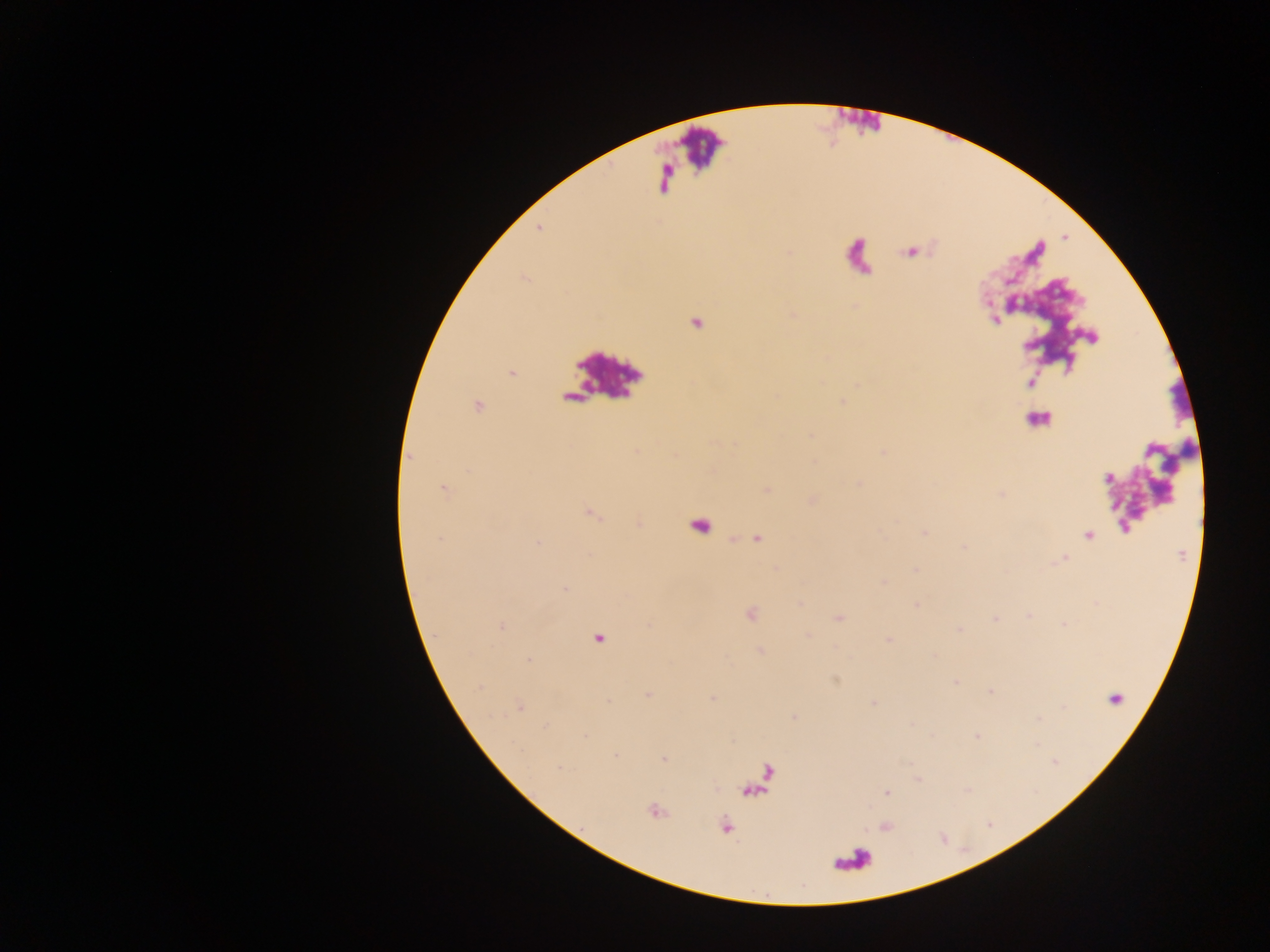
preparation = thick blood smear
Plasmodium parasite locations = approximate centers as (x, y) in pixels: (538, 227), (511, 373), (477, 406), (442, 488), (766, 490), (590, 512), (924, 533), (1088, 535), (757, 537), (1064, 559), (915, 568), (566, 589), (916, 604), (750, 613), (838, 616), (501, 626), (599, 638), (888, 640), (956, 681), (989, 691), (647, 694), (712, 697), (1114, 699), (874, 702), (518, 706), (794, 717), (977, 735), (615, 756), (662, 759), (886, 792), (654, 811), (725, 827)
country = Ghana
capture = mobile-phone photograph through a microscope
field of view = single
image size = 1270×952 pixels
leukocyte locations = approximate centers as (x, y) in pixels: (603, 376), (1037, 420), (699, 526), (851, 860)